Give the preparation type.
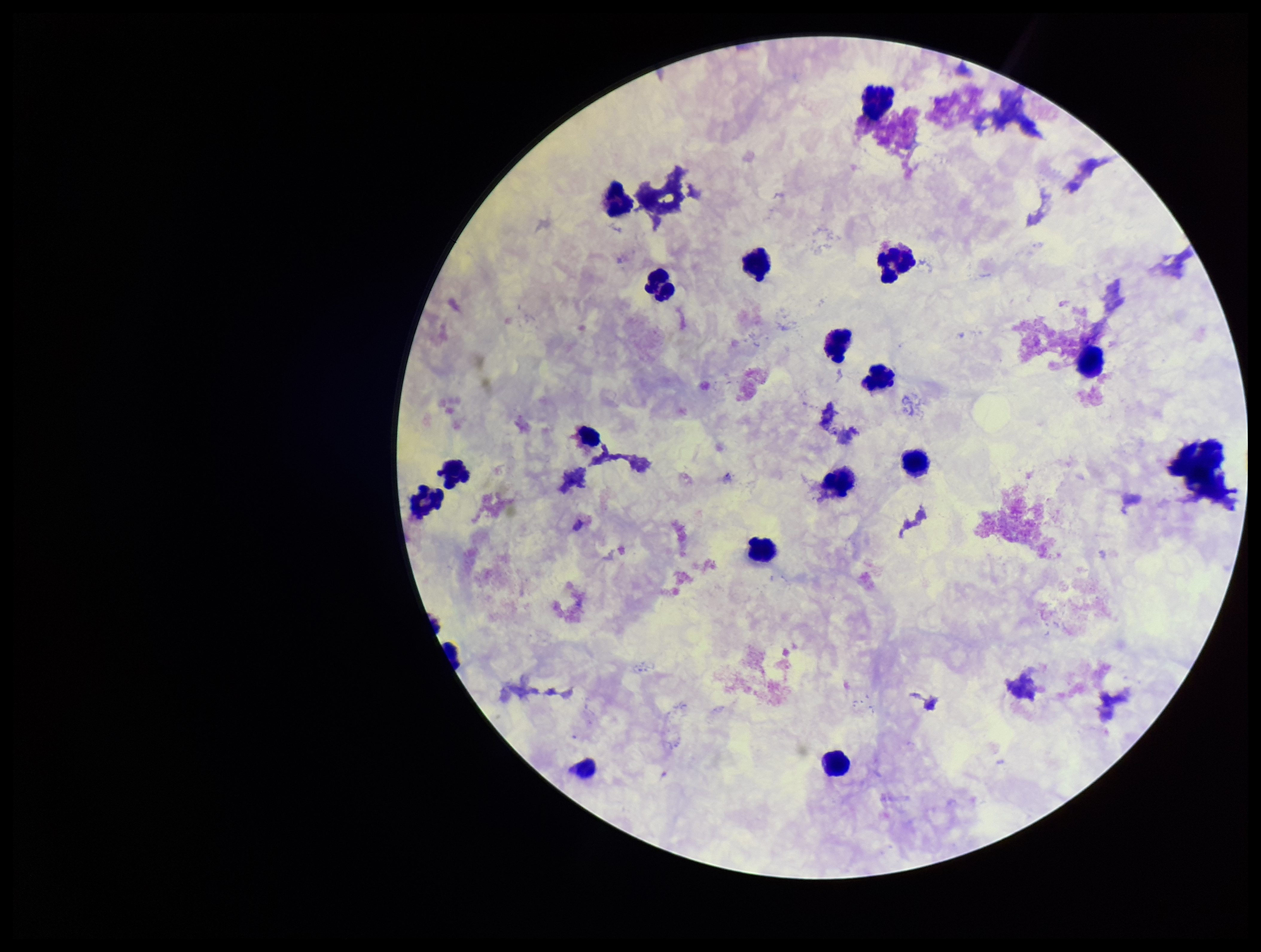
A thick smear.

Image is 1261×952 pixels. Leukocyte count: 15. Parasite count: 0. One field from this slide. Patient malaria status: negative. Plasmodium parasites: none seen. Giemsa stain. Photographed through the microscope eyepiece with a smartphone camera.